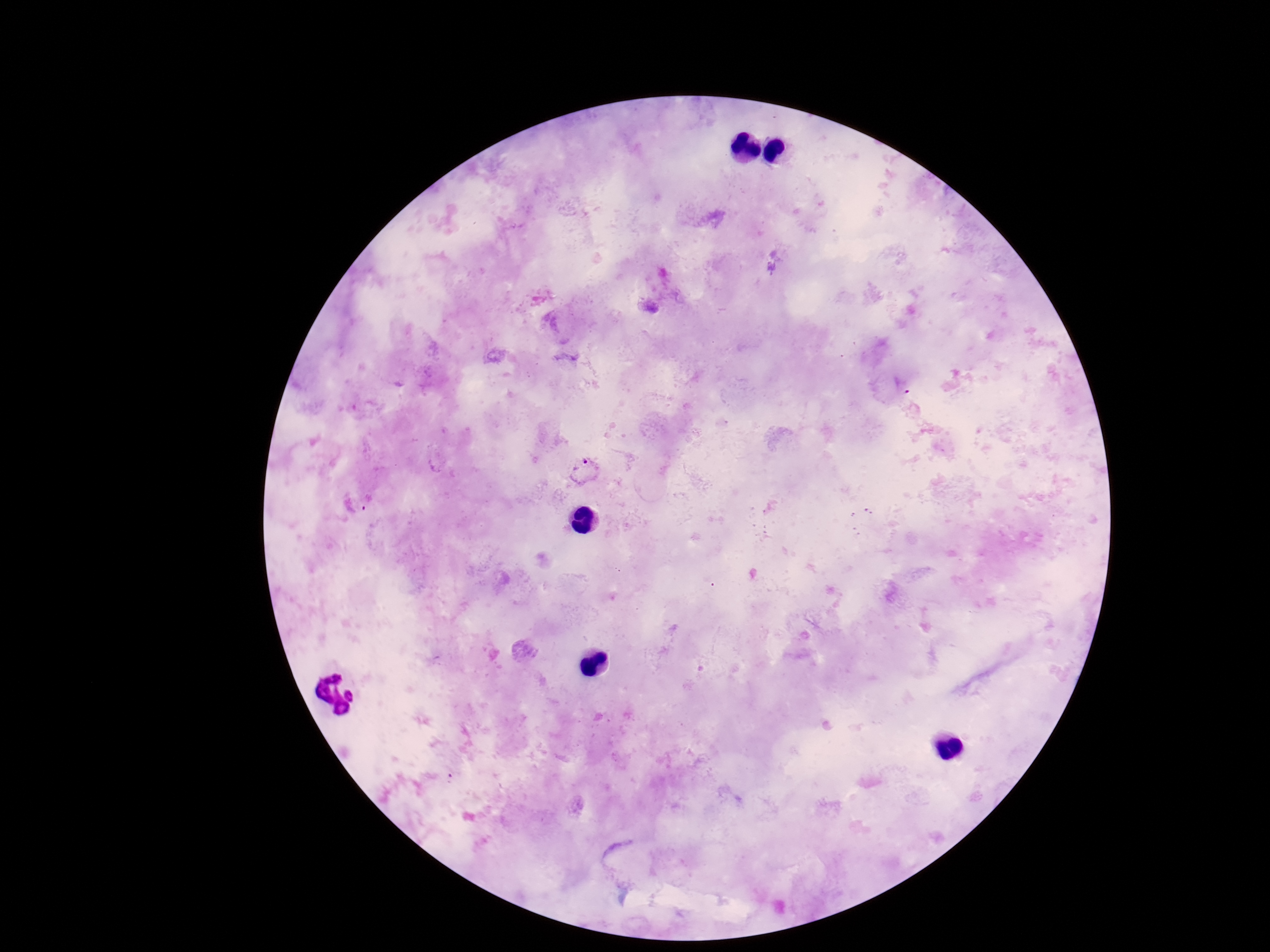 Approximate centers as (x, y) in pixels. Plasmodium parasite locations: (902, 386), (585, 470), (368, 504). Patient malaria status: infected. 100x magnification. One field from this slide. Smartphone photograph taken through the microscope eyepiece. Giemsa-stained preparation. Image is 1270×952 pixels. Thick blood film.